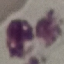 Result: no malaria parasites seen. Cell patch, automatically extracted from a larger field of view and resized to 64 × 64 pixels. Thin blood film. Giemsa stain. Photographed with a smartphone camera at the microscope eyepiece.